Assess the background quality.
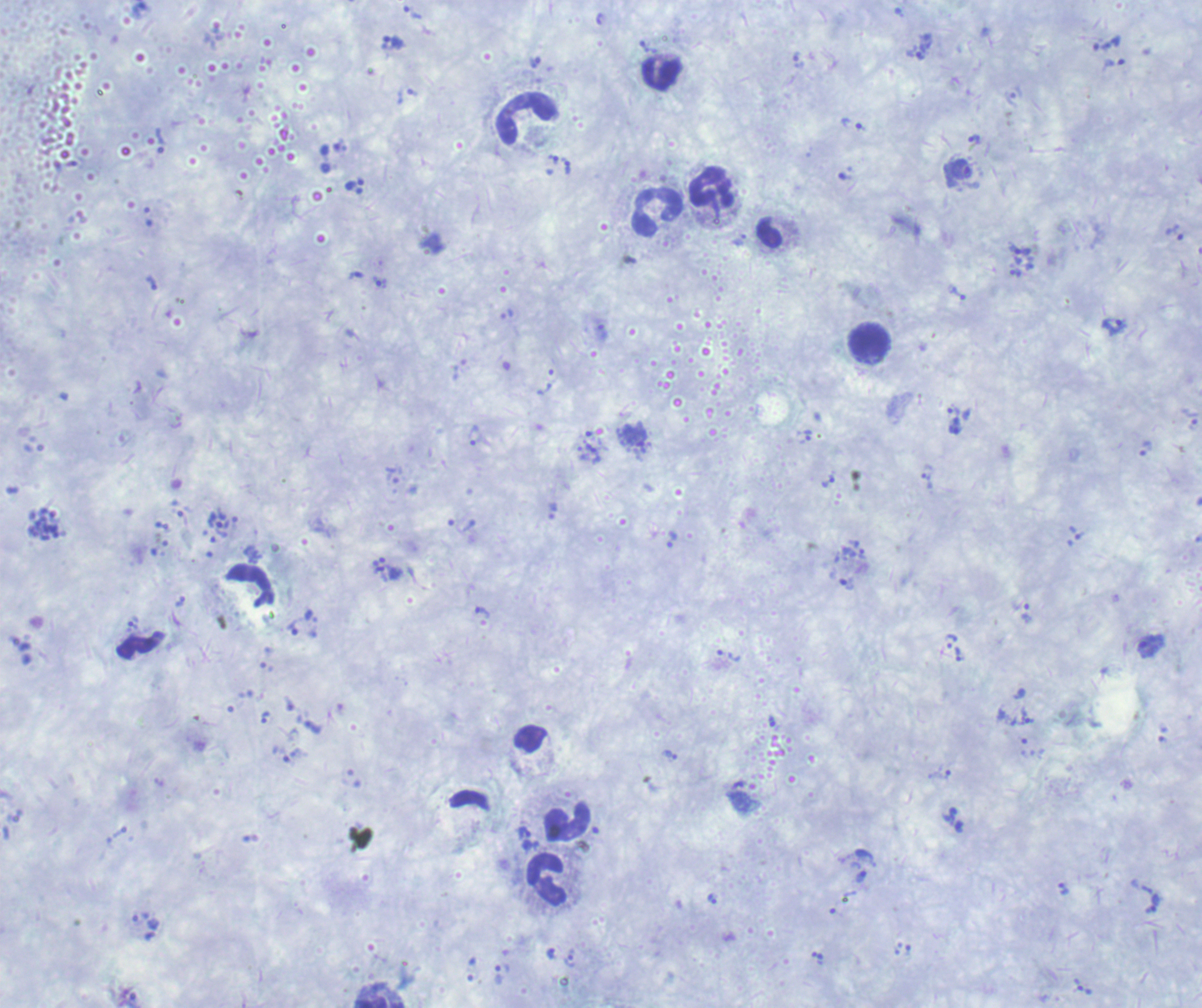
It is poor.

Approximate object centers, in pixels from the top-left corner. Leukocyte locations: (x=661, y=74), (x=526, y=119), (x=713, y=188), (x=658, y=213), (x=869, y=342), (x=569, y=823), (x=548, y=879), (x=379, y=1003). Schizont locations: (x=44, y=524). Trophozoite locations: (x=412, y=12), (x=394, y=42), (x=920, y=56), (x=535, y=62), (x=853, y=124), (x=974, y=138), (x=161, y=141), (x=568, y=167), (x=959, y=170), (x=355, y=184), (x=1176, y=232), (x=1021, y=250), (x=381, y=282), (x=958, y=293), (x=1114, y=325), (x=953, y=410), (x=1191, y=417), (x=956, y=426), (x=635, y=434), (x=806, y=436), (x=1146, y=449), (x=926, y=480), (x=828, y=482), (x=222, y=529), (x=672, y=538), (x=483, y=612), (x=1028, y=614), (x=293, y=629), (x=951, y=641), (x=1151, y=645), (x=729, y=655), (x=960, y=655), (x=264, y=717), (x=1027, y=717), (x=670, y=755), (x=524, y=833), (x=1063, y=889), (x=1154, y=904), (x=571, y=961), (x=498, y=975). Life-cycle stages observed: trophozoite, schizont. Captured at 100x magnification. Result: positive for malaria parasites. Image is 1202×1008 pixels. Previously used in an actual diagnosis. Thick blood smear. Romanowsky stain. One field from this slide.